State which parasite is depicted.
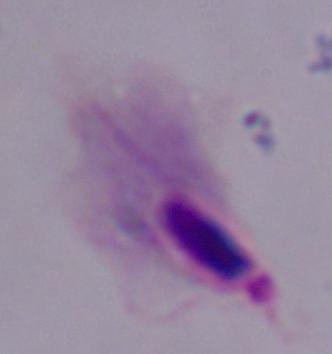

This is a trichomonad.

Summary:
  - Magnification: 1000x
  - Modality: photomicrograph